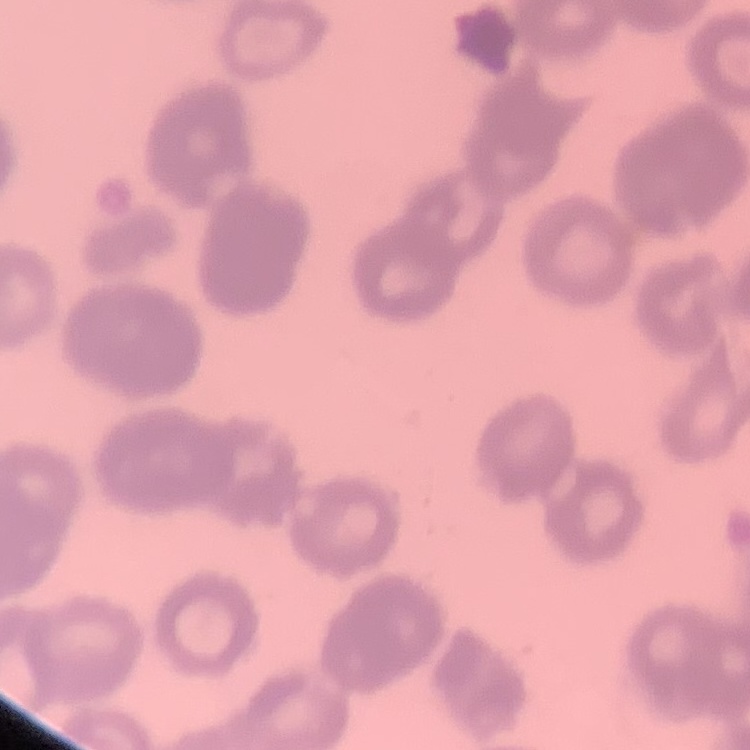

Summary:
  - Erythrocyte morphology: rouleaux formation
  - Stain: Field's or Giemsa
  - Image type: one tile cut from a larger photomicrograph
  - Preparation: thin blood smear